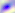

identification: Toxoplasma gondii
modality: micrograph
magnification: 400x